Classify this cell by malaria status.
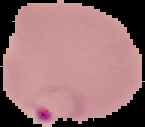

It is parasitized.

image type = cell region segmented out of the field of view; surrounding area masked to black
preparation = thin blood smear
image size = 145×127 pixels